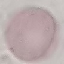

Result: no malaria parasites detected. Photographed with a smartphone camera at the microscope eyepiece. Cell patch, automatically extracted from a larger field of view and resized to 64 × 64 pixels. Thin smear of blood. Giemsa-stained preparation.